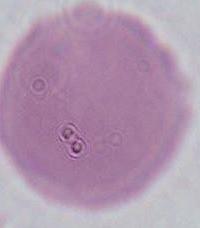
Micrograph. 1000x magnification. An erythrocyte is shown.